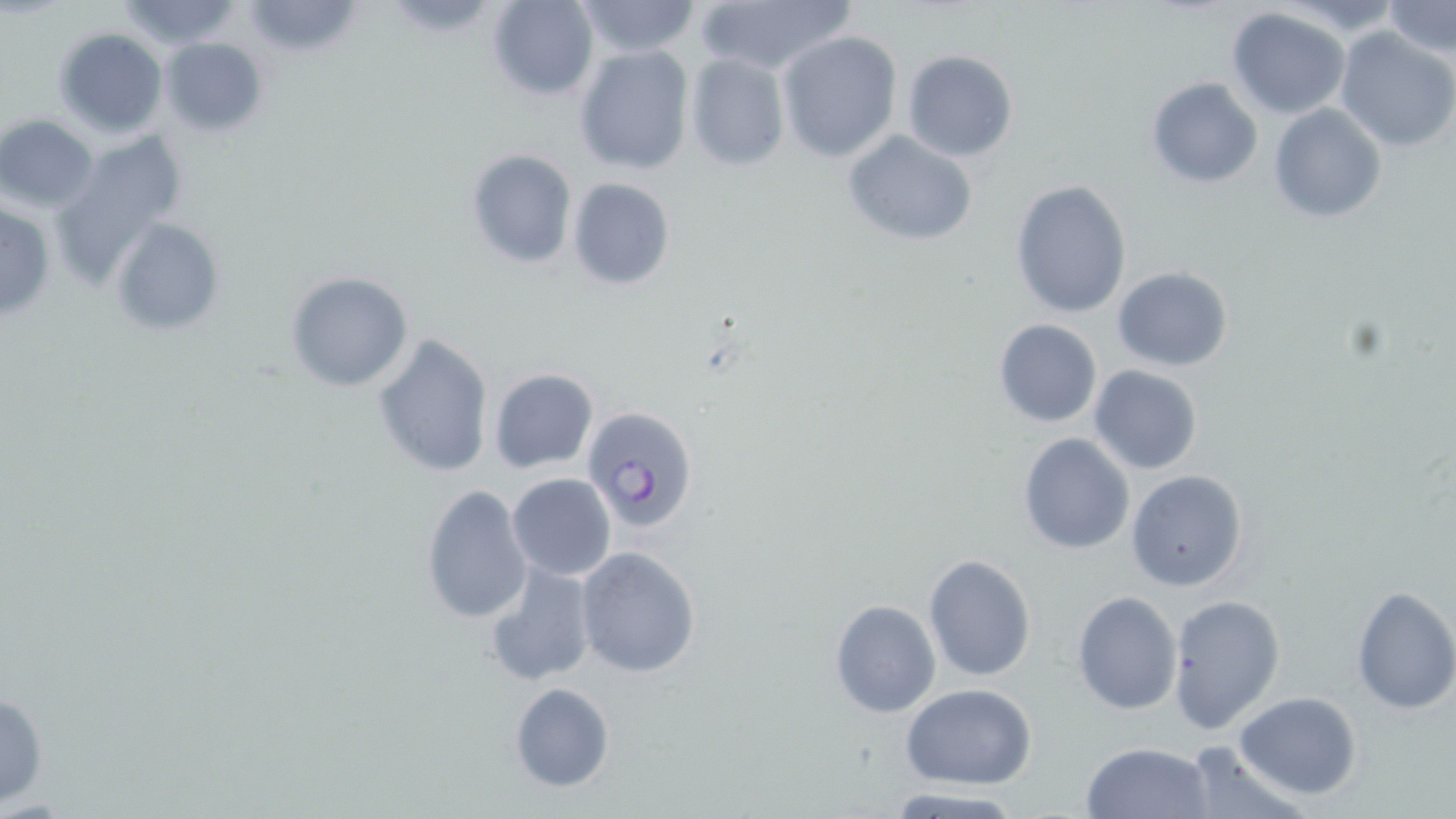

Summary:
  - Coordinate format: approximate bounding boxes as (x1, y1, x2, y2) in pixels
  - Uninfected red blood cell locations: (112, 0, 246, 47), (485, 0, 599, 101), (572, 0, 703, 58), (1283, 0, 1402, 35), (240, 1, 366, 60), (692, 1, 854, 78), (1383, 1, 1455, 56), (1226, 7, 1352, 118), (1334, 26, 1456, 152), (53, 27, 168, 137), (776, 30, 903, 162), (158, 37, 268, 138), (574, 44, 694, 175), (902, 50, 1018, 162), (685, 53, 790, 171), (1143, 75, 1264, 189), (1269, 103, 1388, 223), (0, 113, 99, 212), (841, 128, 980, 248), (52, 137, 186, 277), (465, 148, 577, 268), (566, 177, 676, 290), (1009, 178, 1133, 319), (0, 200, 56, 322), (111, 217, 227, 339), (1113, 266, 1235, 371), (284, 272, 414, 393), (993, 318, 1104, 428), (370, 333, 495, 479), (1088, 365, 1205, 475), (487, 368, 598, 474), (1017, 432, 1136, 555), (1127, 470, 1248, 592), (506, 473, 616, 581), (419, 484, 532, 625), (575, 546, 702, 678), (922, 553, 1036, 683), (482, 559, 596, 687), (843, 585, 1042, 708), (1349, 585, 1456, 716), (1072, 590, 1181, 714), (1167, 595, 1285, 735), (830, 599, 940, 718), (509, 682, 616, 791), (901, 682, 1037, 787), (0, 688, 49, 808), (1233, 691, 1363, 800), (1176, 739, 1307, 819), (1081, 742, 1214, 819), (883, 788, 1031, 817)
  - Plasmodium falciparum-infected red blood cell locations: (582, 407, 700, 534)
  - Slide-level diagnosis: Plasmodium falciparum
  - Field of view: one of a larger specimen
  - Modality: optical microscopy
  - Preparation: thin blood smear
  - Magnification: 1000x
  - Image size: 1456×819 pixels
  - Stain: May-Grünwald-Giemsa